Locate every leukocyte (white blood cell).
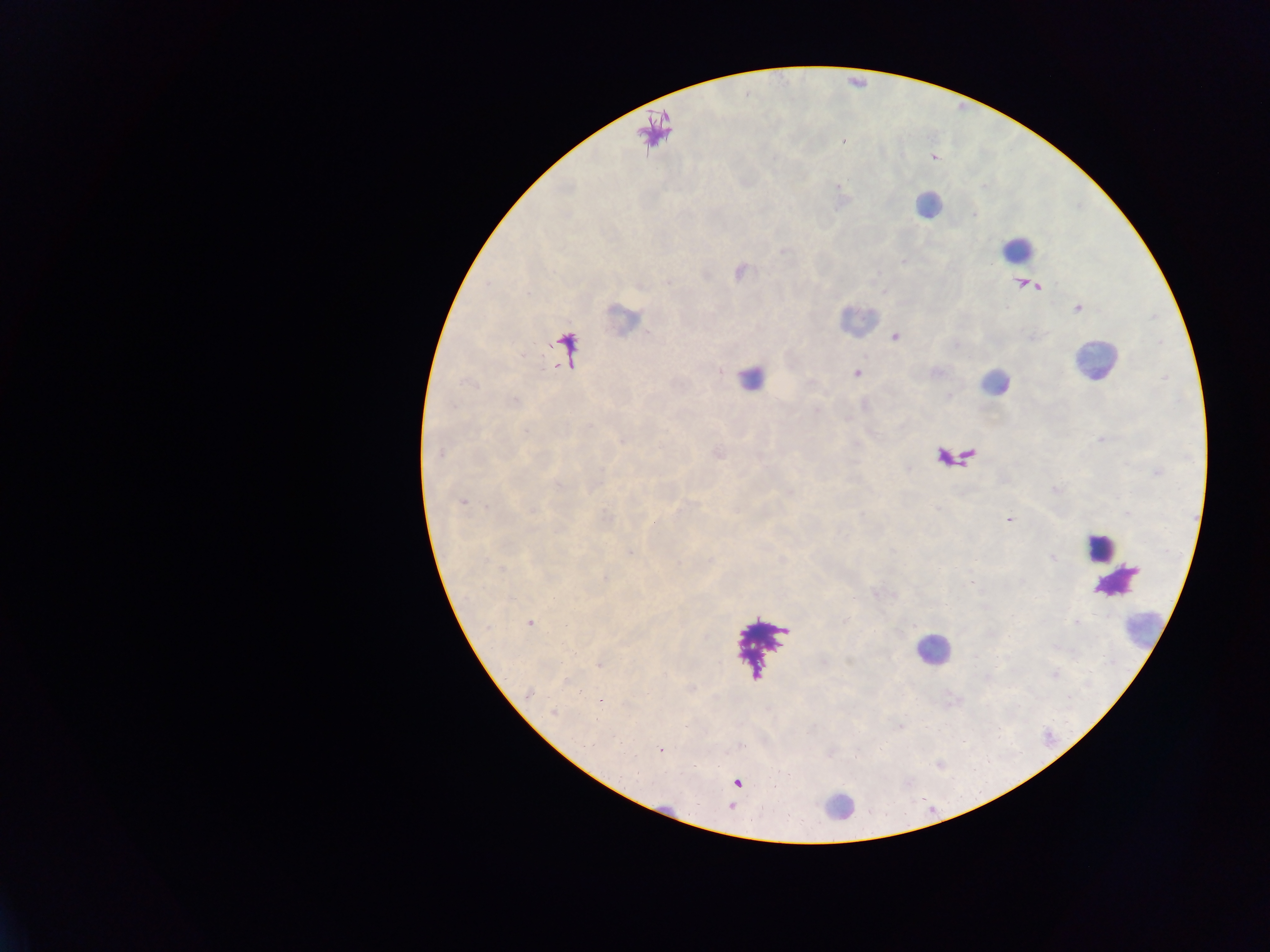

Approximate centers as [x, y] in pixels.
Leukocytes: [927, 204], [1015, 248], [1093, 362], [747, 377], [994, 382], [1097, 547], [1145, 629], [931, 650], [836, 810].

country: Ghana
image_size: 1270×952 pixels
field_of_view: single
malaria_parasite_locations: 'approximate centers as [x, y] in pixels: [856, 373], [461, 501], [1009, 520], [606, 578], [530, 623], [565, 625], [600, 701], [552, 713], [661, 750]'
preparation: thick blood smear
capture: mobile-phone photograph through a microscope